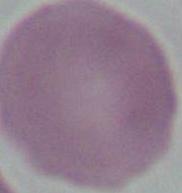
magnification = 1000x
modality = photomicrograph
identification = red blood cell